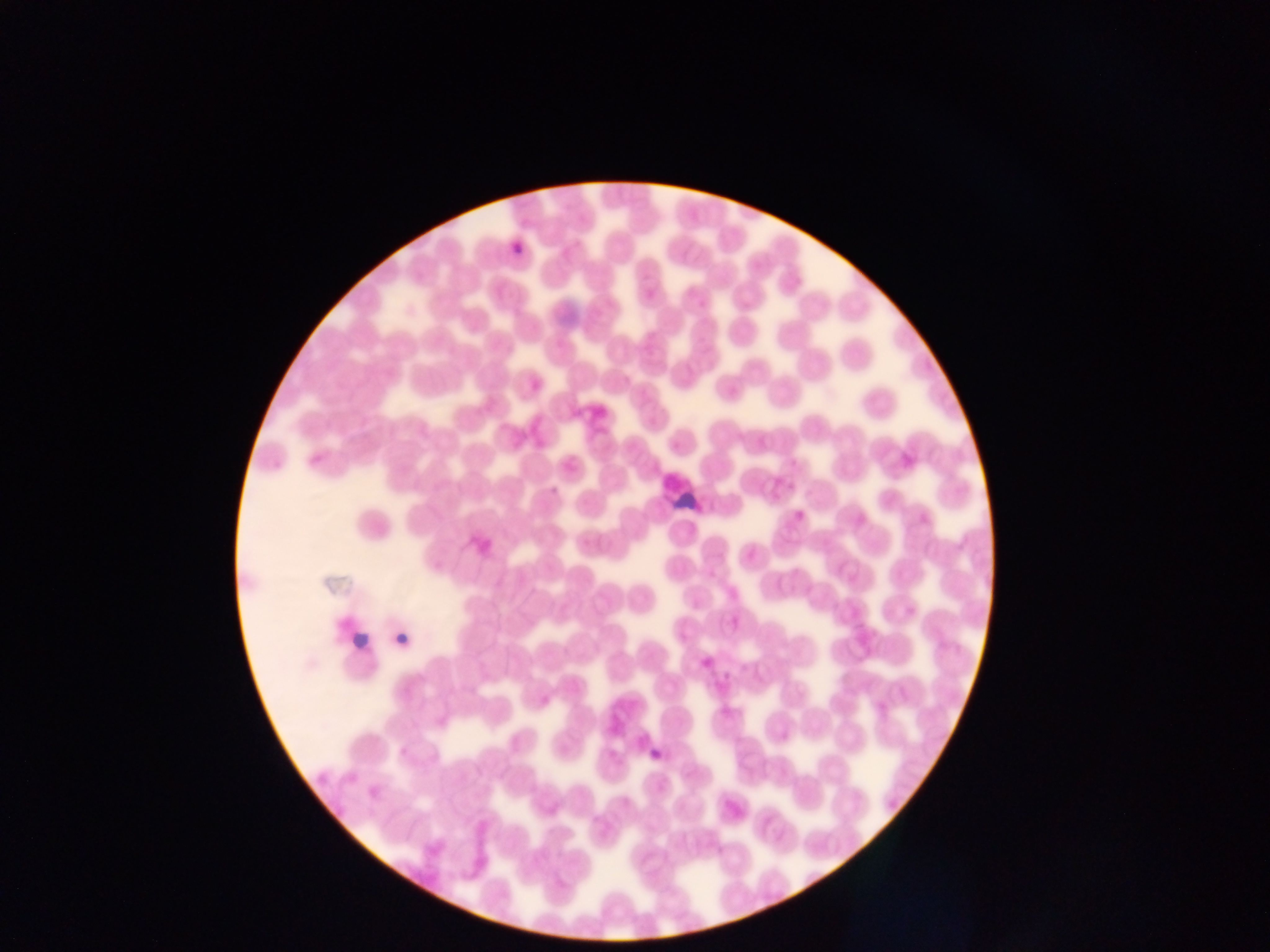
capture: mobile-phone photograph through a microscope
field_of_view: single
country: Ghana
image_size: 1270×952 pixels
plasmodium_parasite_locations: 'approximate bounding boxes as {left, top, right, bottom} in pixels: {510, 243, 528, 256}, {545, 481, 564, 496}, {791, 510, 812, 525}, {394, 622, 416, 649}, {698, 650, 714, 670}, {646, 732, 670, 762}'
preparation: thin blood smear